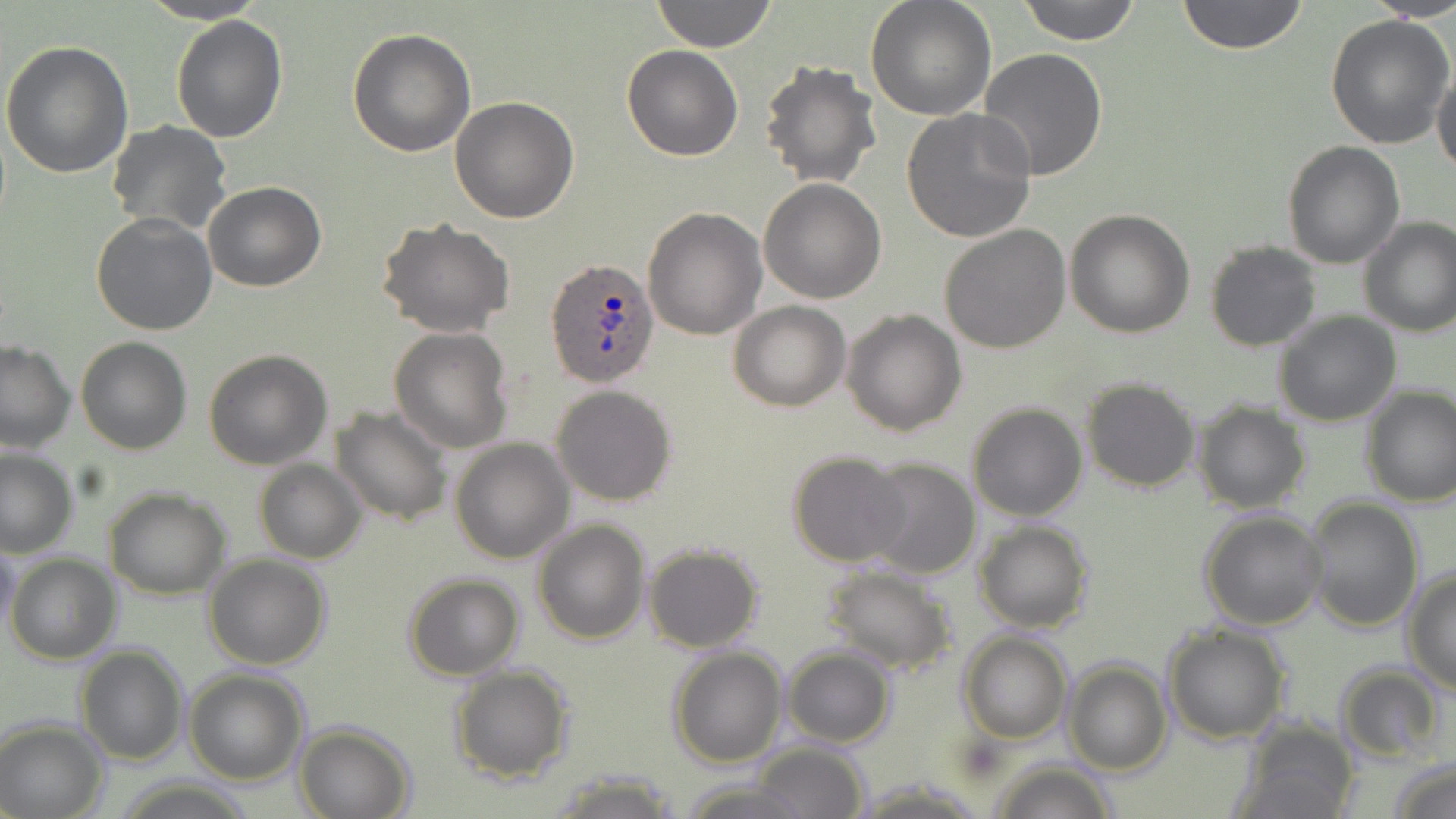

slide-level diagnosis = Plasmodium ovale
magnification = 1000x
Plasmodium ovale-infected red blood cell locations = approximate bounding boxes as named x1/y1/x2/y2 corners in pixels: (x1=545, y1=257, x2=659, y2=388)
field of view = one of a larger specimen
modality = light microscopy
preparation = thin blood film
uninfected red blood cell locations = approximate bounding boxes as named x1/y1/x2/y2 corners in pixels: (x1=139, y1=0, x2=270, y2=24), (x1=651, y1=0, x2=777, y2=52), (x1=866, y1=0, x2=997, y2=121), (x1=1015, y1=0, x2=1144, y2=45), (x1=1176, y1=0, x2=1310, y2=54), (x1=1371, y1=0, x2=1456, y2=19), (x1=1325, y1=11, x2=1456, y2=149), (x1=170, y1=14, x2=288, y2=142), (x1=347, y1=27, x2=475, y2=157), (x1=1, y1=41, x2=134, y2=178), (x1=622, y1=45, x2=743, y2=161), (x1=976, y1=47, x2=1108, y2=181), (x1=760, y1=61, x2=884, y2=190), (x1=1431, y1=63, x2=1456, y2=180), (x1=450, y1=96, x2=581, y2=223), (x1=902, y1=108, x2=1038, y2=242), (x1=107, y1=121, x2=233, y2=235), (x1=1281, y1=141, x2=1405, y2=267), (x1=759, y1=178, x2=887, y2=303), (x1=202, y1=180, x2=326, y2=292), (x1=643, y1=206, x2=767, y2=341), (x1=1065, y1=208, x2=1195, y2=337), (x1=91, y1=212, x2=217, y2=335), (x1=1358, y1=215, x2=1456, y2=337), (x1=377, y1=217, x2=515, y2=337), (x1=940, y1=223, x2=1072, y2=353), (x1=1204, y1=242, x2=1321, y2=352), (x1=729, y1=300, x2=852, y2=411), (x1=841, y1=308, x2=967, y2=436), (x1=1273, y1=310, x2=1402, y2=426), (x1=388, y1=326, x2=514, y2=452), (x1=76, y1=337, x2=193, y2=455), (x1=0, y1=338, x2=77, y2=452), (x1=203, y1=349, x2=332, y2=469), (x1=1079, y1=377, x2=1199, y2=493), (x1=1359, y1=384, x2=1456, y2=507), (x1=550, y1=385, x2=677, y2=506), (x1=1190, y1=399, x2=1312, y2=514), (x1=966, y1=401, x2=1087, y2=520), (x1=331, y1=405, x2=454, y2=528), (x1=449, y1=438, x2=575, y2=564), (x1=0, y1=448, x2=77, y2=557), (x1=787, y1=452, x2=912, y2=568), (x1=860, y1=456, x2=982, y2=580), (x1=255, y1=460, x2=368, y2=563), (x1=104, y1=488, x2=231, y2=599), (x1=1302, y1=497, x2=1424, y2=633), (x1=1199, y1=508, x2=1327, y2=628), (x1=533, y1=519, x2=650, y2=645), (x1=975, y1=520, x2=1094, y2=633), (x1=1, y1=539, x2=21, y2=649), (x1=641, y1=542, x2=764, y2=654), (x1=5, y1=552, x2=121, y2=663), (x1=204, y1=553, x2=333, y2=670), (x1=820, y1=565, x2=957, y2=677), (x1=1401, y1=568, x2=1456, y2=695), (x1=403, y1=572, x2=525, y2=680), (x1=1161, y1=621, x2=1292, y2=743), (x1=957, y1=631, x2=1074, y2=743), (x1=76, y1=644, x2=188, y2=766), (x1=668, y1=646, x2=786, y2=768), (x1=782, y1=646, x2=896, y2=748), (x1=1063, y1=659, x2=1171, y2=775), (x1=1334, y1=663, x2=1446, y2=763), (x1=449, y1=664, x2=573, y2=784), (x1=183, y1=669, x2=310, y2=785), (x1=0, y1=717, x2=108, y2=819), (x1=1235, y1=719, x2=1360, y2=819), (x1=293, y1=722, x2=414, y2=819), (x1=751, y1=743, x2=870, y2=818), (x1=1386, y1=755, x2=1456, y2=819), (x1=989, y1=761, x2=1118, y2=819), (x1=547, y1=770, x2=681, y2=817), (x1=677, y1=779, x2=815, y2=819), (x1=848, y1=779, x2=989, y2=816)
image size = 1456×819 pixels
stain = May-Grünwald-Giemsa